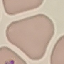 Result: no malaria parasites seen. Giemsa stain. Automatically extracted cell patch, resized to 64 × 64 pixels. Thin blood film. Acquired by smartphone through the microscope eyepiece.